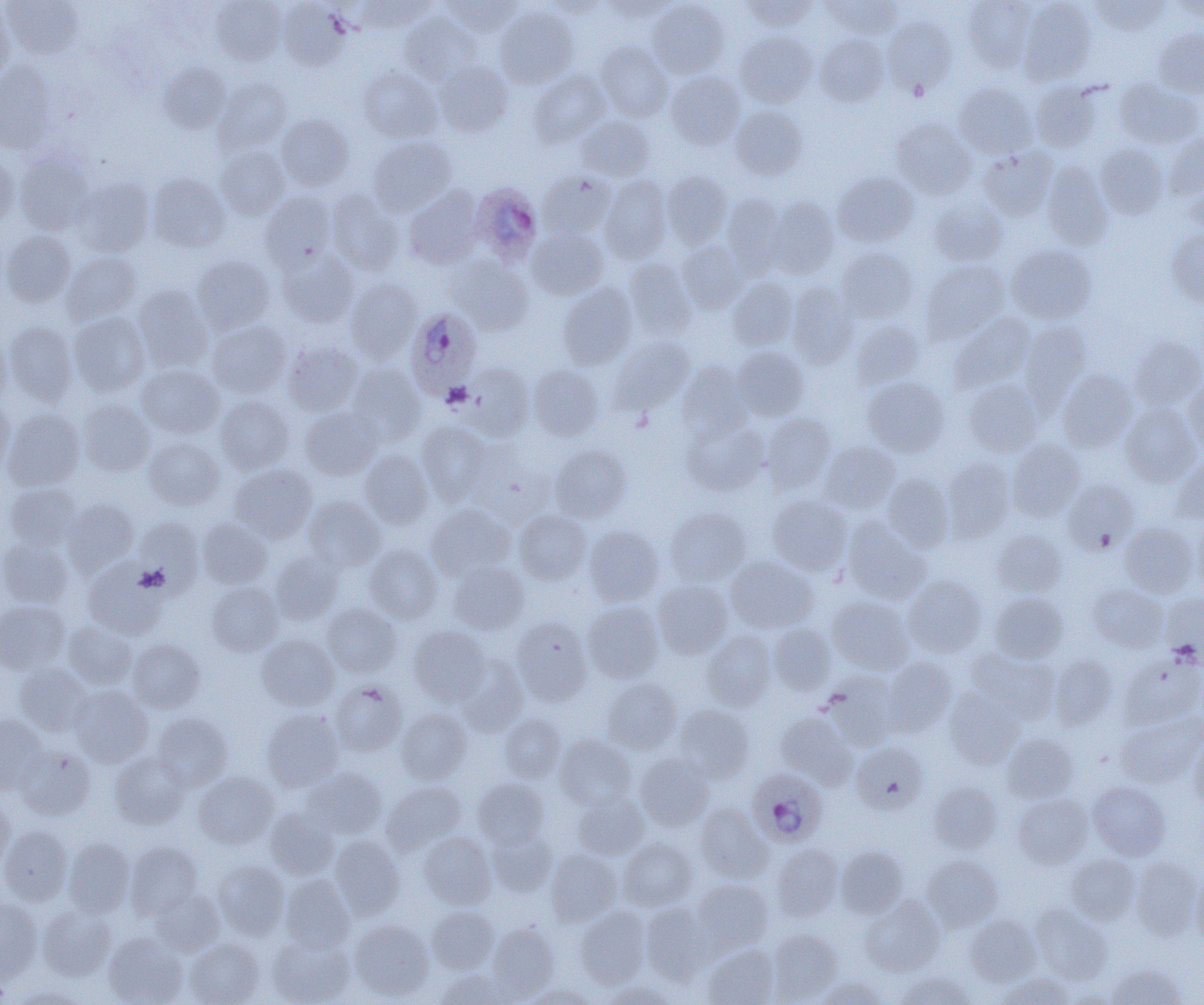

Approximate bounding boxes as (x1, y1, x2, y2) in pixels. Uninfected red blood cell locations: (2, 0, 83, 60), (211, 0, 286, 66), (356, 0, 434, 32), (444, 0, 522, 35), (742, 0, 817, 30), (823, 0, 901, 39), (962, 0, 1038, 71), (1091, 0, 1169, 36), (279, 1, 352, 70), (541, 1, 606, 19), (601, 1, 678, 21), (648, 1, 728, 78), (1019, 1, 1097, 84), (1169, 1, 1204, 23), (0, 5, 13, 83), (495, 6, 578, 88), (400, 13, 481, 84), (883, 15, 958, 96), (1154, 29, 1204, 97), (735, 32, 817, 107), (815, 34, 889, 106), (596, 42, 673, 121), (433, 61, 512, 137), (0, 62, 57, 153), (158, 63, 230, 133), (358, 66, 442, 141), (529, 69, 611, 146), (666, 71, 745, 149), (214, 78, 291, 153), (1114, 79, 1202, 149), (1030, 81, 1104, 152), (954, 83, 1037, 158), (730, 106, 807, 180), (276, 114, 355, 190), (576, 115, 655, 181), (892, 118, 976, 199), (1164, 133, 1204, 201), (368, 136, 456, 215), (1094, 143, 1168, 219), (215, 145, 290, 219), (978, 146, 1057, 220), (0, 153, 18, 230), (15, 153, 93, 235), (1042, 163, 1112, 249), (662, 171, 732, 247), (537, 172, 615, 239), (832, 172, 918, 247), (147, 173, 229, 252), (599, 176, 671, 263), (73, 177, 154, 256), (403, 186, 483, 268), (326, 189, 402, 274), (260, 191, 337, 269), (722, 193, 788, 275), (928, 196, 1008, 266), (767, 197, 838, 278), (528, 227, 608, 299), (1166, 228, 1204, 307), (1, 231, 75, 306), (677, 241, 748, 313), (1007, 245, 1097, 324), (835, 247, 917, 322), (276, 249, 358, 326), (61, 252, 141, 324), (193, 255, 274, 333), (449, 256, 533, 335), (624, 258, 697, 339), (922, 260, 1009, 342), (728, 277, 798, 349), (346, 279, 422, 362), (787, 283, 859, 367), (558, 284, 636, 369), (133, 286, 212, 371), (70, 312, 150, 396), (949, 313, 1034, 394), (207, 320, 291, 397), (851, 320, 924, 388), (1020, 320, 1092, 406), (4, 321, 77, 405), (0, 333, 9, 410), (1129, 335, 1204, 410), (609, 337, 694, 413), (283, 340, 363, 415), (732, 346, 808, 420), (678, 361, 752, 440), (461, 363, 534, 439), (347, 364, 426, 444), (137, 365, 224, 438), (528, 365, 603, 440), (1058, 369, 1137, 452), (863, 377, 949, 456), (964, 379, 1043, 456), (1184, 379, 1204, 456), (215, 395, 295, 474), (0, 399, 14, 476), (78, 400, 155, 476), (1120, 403, 1201, 486), (300, 406, 381, 479), (2, 409, 85, 490), (761, 412, 835, 493), (682, 418, 768, 496), (416, 421, 492, 505), (144, 437, 224, 510), (1007, 440, 1085, 520), (820, 441, 900, 513), (469, 443, 555, 527), (550, 444, 632, 522), (359, 451, 432, 529), (1170, 455, 1204, 525), (941, 458, 1014, 542), (230, 464, 316, 543), (883, 473, 954, 551), (1063, 479, 1139, 554), (5, 483, 81, 549), (768, 495, 851, 576), (304, 496, 386, 572), (63, 499, 138, 575), (426, 504, 513, 580), (665, 508, 751, 585), (514, 511, 591, 584), (1191, 516, 1204, 593), (135, 517, 204, 592), (842, 518, 930, 603), (197, 519, 272, 589), (1120, 522, 1198, 597), (584, 526, 663, 605), (991, 528, 1066, 597), (0, 536, 72, 607), (364, 544, 442, 623), (270, 551, 344, 624), (727, 556, 818, 633), (449, 562, 529, 634), (83, 564, 169, 638), (903, 575, 987, 656), (653, 579, 733, 658), (207, 582, 283, 656), (1088, 584, 1167, 652), (989, 592, 1068, 663), (1161, 593, 1204, 663), (827, 596, 915, 674), (0, 600, 69, 673), (583, 601, 664, 683), (322, 603, 401, 677), (511, 617, 593, 705), (63, 621, 138, 688), (769, 623, 836, 695), (409, 626, 491, 706), (703, 631, 776, 711), (256, 634, 338, 711), (127, 639, 206, 713), (966, 647, 1060, 723), (455, 654, 528, 735), (1119, 654, 1204, 728), (1049, 655, 1117, 729), (881, 657, 958, 735), (15, 663, 92, 736), (822, 672, 900, 749), (602, 679, 681, 753), (330, 680, 407, 756), (70, 686, 153, 767), (945, 689, 1024, 769), (673, 704, 754, 782), (396, 708, 472, 784), (262, 709, 344, 791), (1117, 712, 1203, 788), (153, 713, 233, 789), (499, 713, 566, 782), (776, 713, 858, 788), (0, 715, 48, 792), (1002, 733, 1079, 802), (555, 734, 635, 809), (1188, 734, 1204, 807), (851, 742, 927, 813), (15, 744, 95, 819), (109, 751, 190, 829), (635, 752, 715, 831), (302, 768, 386, 839), (193, 771, 278, 849), (473, 778, 549, 848), (382, 781, 466, 854), (929, 781, 1002, 853), (1088, 781, 1170, 860), (573, 791, 649, 859), (1013, 794, 1092, 867), (0, 797, 15, 870), (696, 802, 773, 882), (265, 809, 338, 879), (0, 826, 72, 905), (487, 829, 556, 897), (419, 832, 495, 908), (330, 836, 405, 919), (63, 837, 135, 917), (619, 838, 697, 910), (126, 842, 203, 918), (772, 844, 844, 921), (836, 845, 908, 918), (546, 850, 621, 926), (1065, 853, 1141, 924), (921, 855, 1003, 931), (1130, 856, 1202, 940), (212, 860, 289, 938), (1190, 870, 1204, 947), (280, 874, 355, 953), (692, 879, 773, 952), (149, 889, 224, 957), (861, 896, 945, 976), (0, 898, 43, 979), (640, 902, 712, 982), (1030, 904, 1112, 984), (38, 906, 116, 980), (575, 906, 651, 987), (427, 907, 498, 973), (965, 914, 1041, 986), (350, 920, 434, 1000), (487, 923, 559, 998), (767, 928, 843, 1002), (104, 932, 187, 1005), (267, 935, 354, 1005), (184, 938, 264, 1005), (702, 945, 778, 1005), (1107, 963, 1187, 1004), (436, 969, 510, 1004), (898, 971, 976, 1005), (998, 971, 1076, 1004), (815, 976, 889, 1005), (602, 981, 677, 1005), (522, 984, 597, 1004), (12, 986, 88, 1004). Plasmodium ovale-infected red blood cell locations: (470, 182, 543, 265), (405, 308, 481, 399), (747, 767, 828, 846). Slide-level diagnosis: Plasmodium ovale. Thin blood smear. Captured at 1000x magnification. Optical microscopy. Single field of view. Image is 1204×1005 pixels.